Classify this cell by malaria status.
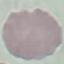

It is uninfected.

capture = smartphone camera at the microscope eyepiece
image type = automatically extracted cell patch, resized to 64 × 64 pixels
stain = Giemsa
preparation = thin blood film